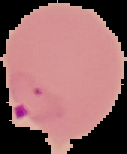
{
  "preparation": "thin blood smear",
  "result": "malaria parasites identified",
  "image_size": "127×154 pixels",
  "image_type": "segmented cell region with the area outside set to black"
}